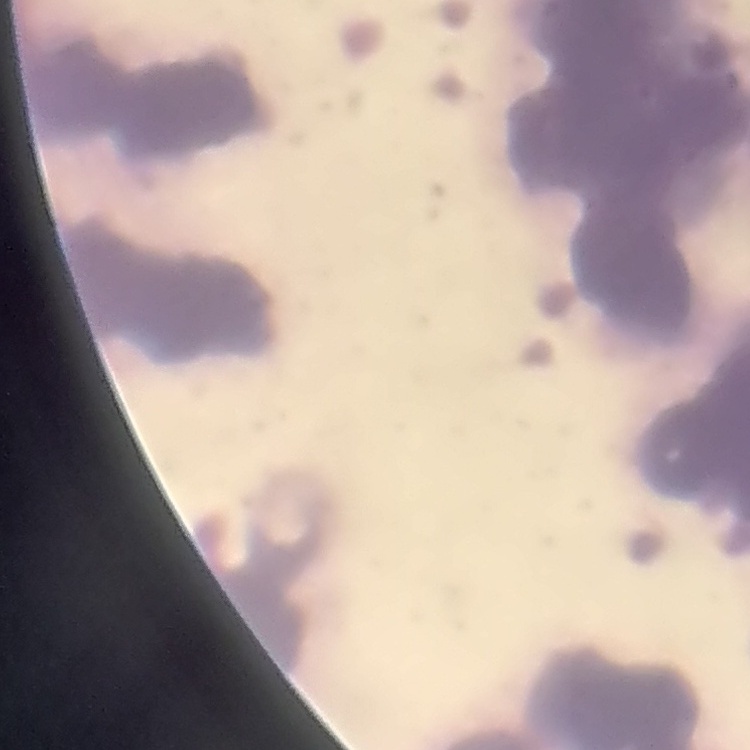
Summary:
  - Erythrocyte morphology: rouleaux formation
  - Preparation: thin blood smear
  - Image type: one tile cut from a larger photomicrograph
  - Stain: Field's or Giemsa